Report the malaria status of this cell.
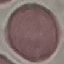
It is uninfected.

preparation = thin blood film
capture = smartphone through the microscope eyepiece
stain = Giemsa
image type = automatically extracted cell patch, resized to 64 × 64 pixels